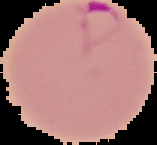

image size = 157×145 pixels
image type = cell region segmented out of the field of view; surrounding area masked to black
result = Plasmodium parasites identified
preparation = thin blood film